Report the malaria status of this cell.
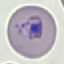

It is parasitized.

preparation = thin smear
capture = smartphone camera at the microscope eyepiece
image type = automatically extracted cell patch, resized to 64 × 64 pixels
stain = Giemsa